Classify this cell by malaria status.
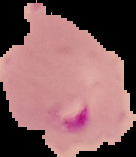

Parasitized.

Summary:
  - Preparation: thin blood smear
  - Image type: segmented cell region on a black background
  - Image size: 136×157 pixels